Identify the blood parasite species.
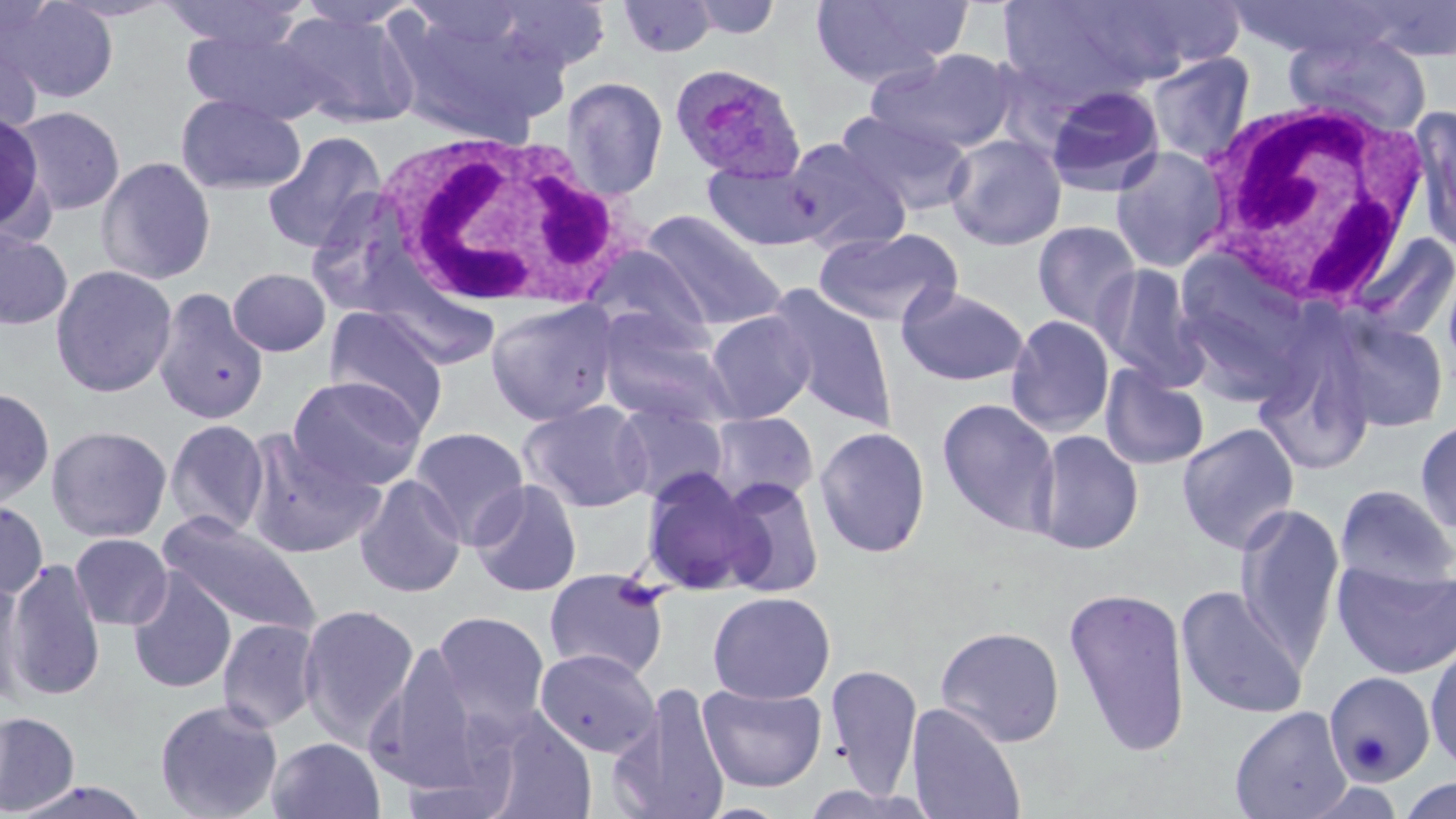
Plasmodium ovale.

Approximate bounding boxes as (x1, y1, x2, y2) in pixels. Uninfected red blood cell locations: (1, 0, 120, 104), (48, 0, 181, 23), (294, 0, 422, 31), (485, 0, 613, 74), (686, 0, 784, 40), (809, 0, 970, 87), (993, 0, 1172, 102), (159, 1, 311, 52), (616, 1, 720, 58), (1351, 3, 1456, 61), (389, 5, 564, 140), (276, 8, 421, 129), (181, 27, 334, 126), (1284, 32, 1433, 138), (0, 34, 43, 144), (865, 48, 1018, 156), (1146, 52, 1256, 163), (560, 77, 669, 198), (175, 92, 306, 196), (8, 104, 127, 216), (1412, 109, 1456, 256), (0, 111, 52, 241), (838, 111, 975, 216), (259, 131, 388, 254), (944, 134, 1067, 251), (783, 137, 912, 255), (1110, 145, 1230, 273), (95, 156, 217, 286), (702, 161, 827, 251), (642, 209, 787, 330), (1032, 220, 1143, 334), (0, 227, 73, 331), (814, 227, 963, 328), (1345, 231, 1454, 346), (583, 244, 715, 349), (1172, 245, 1324, 403), (1092, 262, 1208, 389), (49, 263, 179, 398), (227, 267, 331, 357), (896, 284, 1030, 386), (768, 285, 899, 431), (152, 288, 269, 425), (485, 298, 620, 426), (324, 307, 449, 434), (596, 310, 735, 428), (704, 310, 816, 423), (1326, 313, 1450, 433), (1005, 314, 1115, 437), (1255, 340, 1376, 476), (1099, 363, 1210, 471), (287, 376, 427, 491), (0, 387, 56, 507), (937, 398, 1060, 535), (519, 400, 653, 513), (612, 403, 729, 505), (707, 411, 819, 507), (1414, 417, 1456, 536), (163, 418, 271, 538), (1176, 423, 1301, 554), (46, 424, 173, 544), (409, 426, 530, 547), (814, 426, 931, 558), (241, 429, 385, 560), (1030, 430, 1144, 555), (640, 470, 761, 595), (354, 475, 467, 599), (715, 477, 826, 599), (469, 479, 583, 597), (1334, 484, 1456, 591), (0, 500, 49, 598), (1234, 502, 1346, 668), (158, 513, 321, 638), (69, 532, 174, 631), (5, 558, 107, 701), (1331, 558, 1456, 680), (542, 568, 671, 682), (126, 570, 237, 694), (0, 577, 28, 708), (1175, 584, 1309, 720), (1063, 585, 1193, 757), (707, 590, 836, 704), (296, 602, 421, 747), (429, 610, 552, 738), (216, 618, 322, 733), (934, 625, 1066, 747), (369, 640, 486, 792), (1425, 641, 1456, 775), (533, 647, 660, 758), (824, 663, 923, 799), (1323, 671, 1436, 786), (608, 682, 732, 819), (697, 682, 828, 792), (153, 698, 284, 819), (905, 702, 1027, 819), (1229, 706, 1352, 819), (473, 708, 598, 819), (0, 710, 80, 816), (265, 736, 386, 819), (1396, 775, 1456, 819), (10, 779, 151, 819). White blood cell locations: (1200, 96, 1438, 313), (369, 128, 635, 311). Plasmodium ovale-infected red blood cell locations: (669, 63, 806, 183). Optical microscopy. One field of a larger specimen. 1000x magnification. Image is 1456×819 pixels. Thin blood film. May-Grünwald-Giemsa-stained preparation.